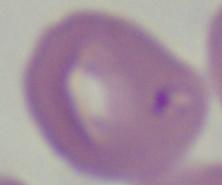
identification = Babesia
modality = photomicrograph
magnification = 1000x